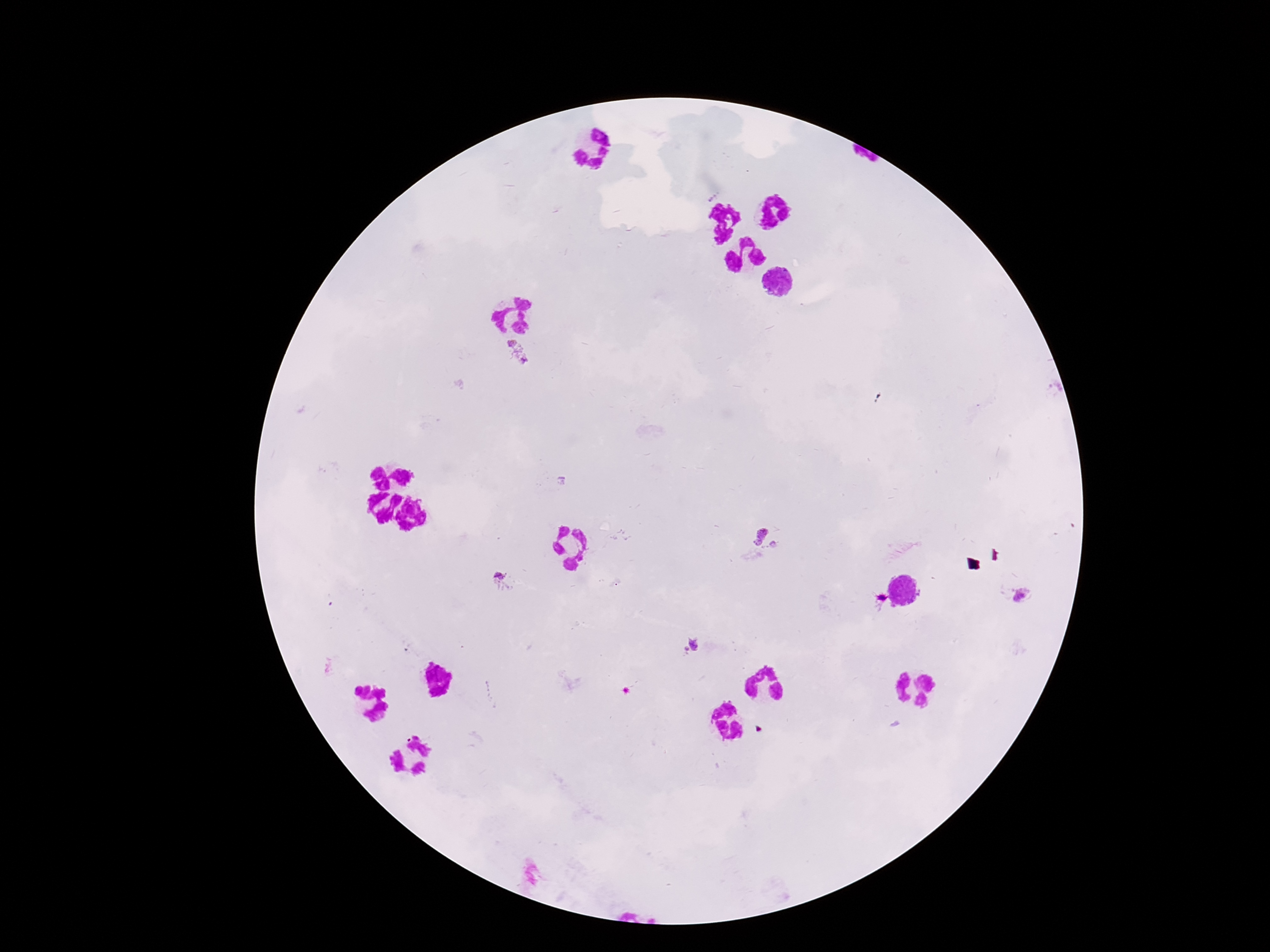
Approximate centers as {x, y} in pixels.
Summary:
  - Plasmodium parasite locations: {518, 353}, {767, 539}, {501, 579}, {1021, 597}, {690, 646}
  - Image size: 1270×952 pixels
  - Stain: Giemsa
  - Magnification: 100x
  - Patient malaria status: infected
  - Field of view: one from this slide
  - Preparation: thick blood film
  - Capture: smartphone camera through the microscope eyepiece